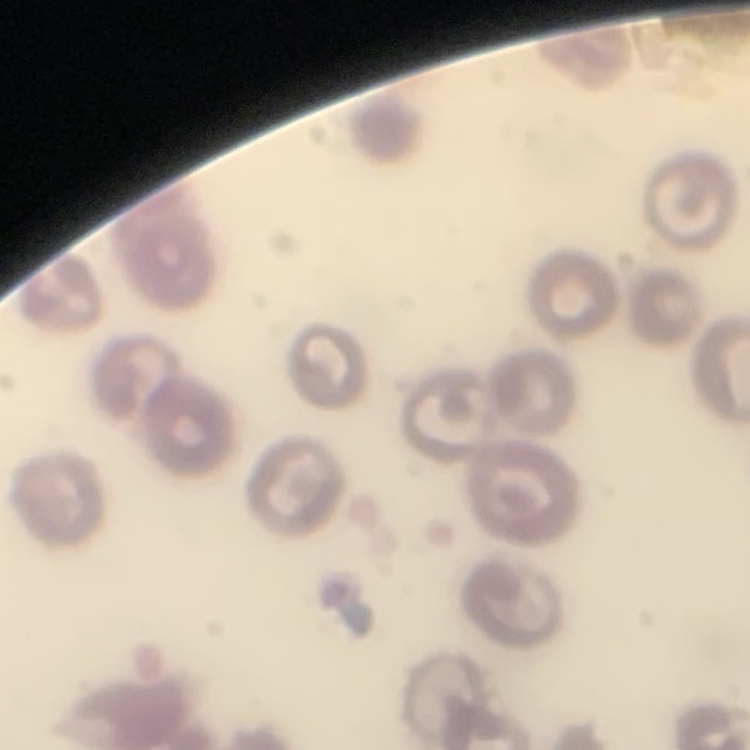
red blood cell morphology = no rouleaux formation
stain = Field's or Giemsa
preparation = thin blood smear
image type = one tile cut from a larger photomicrograph